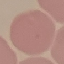

Summary:
  - Malaria status: uninfected
  - Preparation: thin blood film
  - Image type: automatically extracted cell patch, resized to 64 × 64 pixels
  - Capture: smartphone through the microscope eyepiece
  - Stain: Giemsa